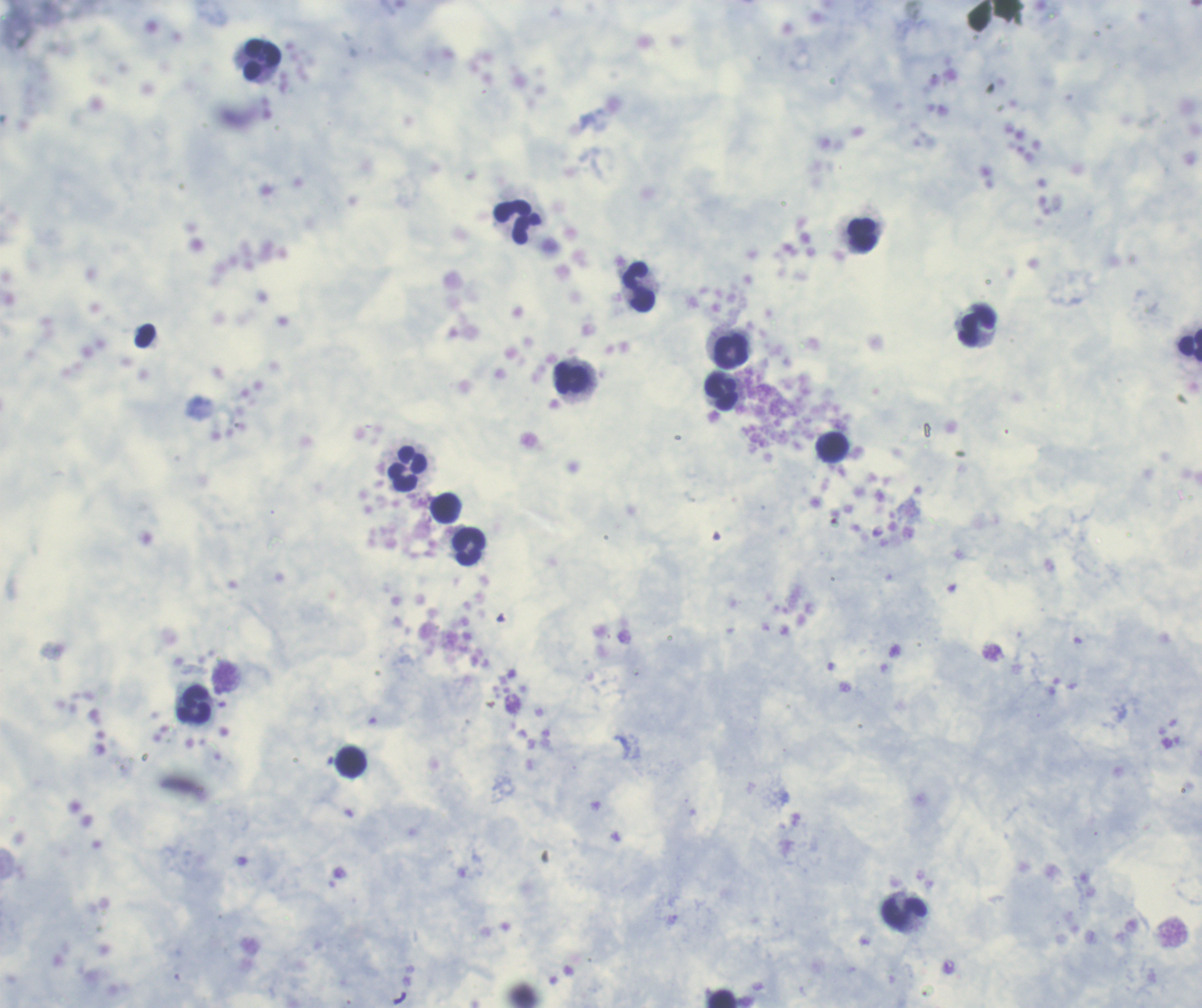
Approximate object centers, in pixels from the top-left corner.
Summary:
  - Leukocyte locations: (x=262, y=60), (x=517, y=224), (x=862, y=235), (x=639, y=287), (x=978, y=326), (x=1190, y=346), (x=731, y=352), (x=572, y=378), (x=721, y=393), (x=833, y=447), (x=407, y=470), (x=445, y=509), (x=469, y=547), (x=194, y=705), (x=351, y=763), (x=903, y=913), (x=724, y=999)
  - Magnification: 100x
  - Coloration quality: good
  - Context: previously used in an actual diagnosis
  - Stain: Romanowsky
  - Image size: 1202×1008 pixels
  - Result: no malaria parasites seen
  - Preparation: thick blood film
  - Field of view: single
  - Background quality: poor